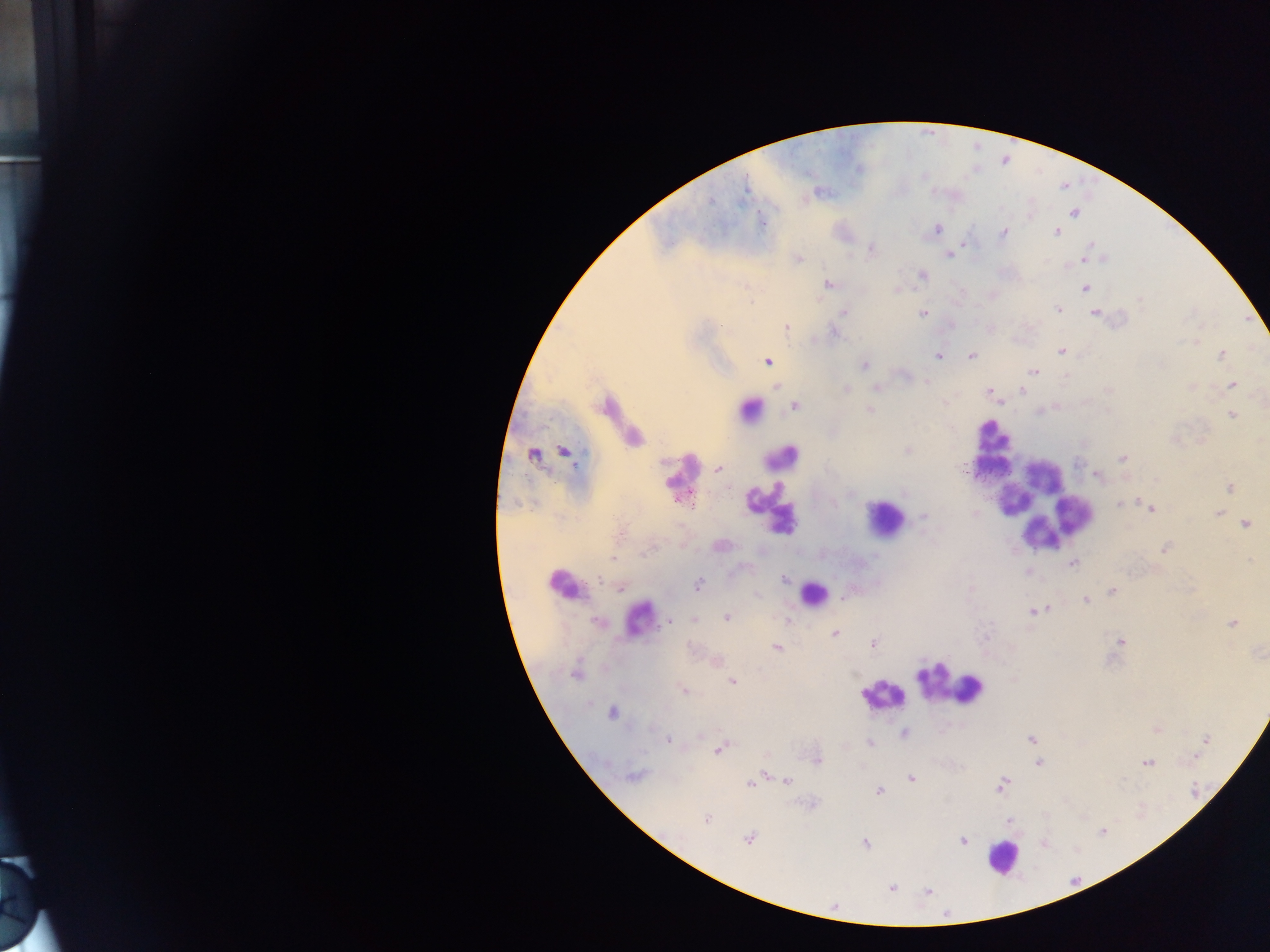
Approximate centers as {x, y} in pixels.
Summary:
  - Plasmodium parasite locations: {744, 188}, {710, 201}, {1074, 213}, {937, 229}, {1057, 232}, {1003, 234}, {965, 242}, {1091, 247}, {872, 249}, {1086, 253}, {949, 254}, {798, 258}, {1082, 259}, {923, 276}, {829, 285}, {1085, 288}, {1057, 310}, {843, 312}, {923, 314}, {1095, 314}, {786, 326}, {835, 332}, {1061, 351}, {1221, 355}, {938, 357}, {971, 357}, {768, 362}, {864, 365}, {1033, 372}, {1232, 384}, {875, 387}, {846, 389}, {1022, 390}, {989, 392}, {794, 406}, {749, 410}, {869, 411}, {1232, 415}, {907, 450}, {564, 452}, {534, 456}, {1122, 458}, {719, 468}, {1096, 476}, {1230, 488}, {1119, 504}, {1151, 508}, {1217, 513}, {923, 517}, {1246, 525}, {720, 546}, {1164, 548}, {613, 558}, {1072, 563}, {1027, 572}, {784, 579}, {600, 580}, {698, 585}, {620, 588}, {1112, 591}, {757, 595}, {1086, 600}, {1034, 612}, {727, 618}, {695, 619}, {786, 620}, {596, 621}, {669, 622}, {1233, 623}, {834, 634}, {1121, 642}, {874, 644}, {776, 648}, {574, 674}, {732, 682}, {684, 690}, {612, 713}, {905, 733}, {1031, 739}, {669, 740}, {1206, 740}, {869, 743}, {720, 749}, {816, 760}, {1147, 763}, {1038, 764}, {634, 775}, {911, 778}, {787, 781}, {750, 784}, {1001, 785}, {879, 791}, {706, 819}, {1009, 821}, {1102, 832}, {749, 840}, {963, 841}, {865, 844}, {892, 888}, {928, 892}
  - Leukocyte locations: {992, 437}, {991, 456}, {782, 458}, {682, 470}, {1036, 502}, {774, 512}, {884, 518}, {565, 584}, {813, 594}, {641, 616}, {949, 683}, {882, 695}, {1003, 857}
  - Capture: mobile-phone photograph through a microscope
  - Preparation: thick blood smear
  - Field of view: single
  - Country: Ghana
  - Image size: 1270×952 pixels